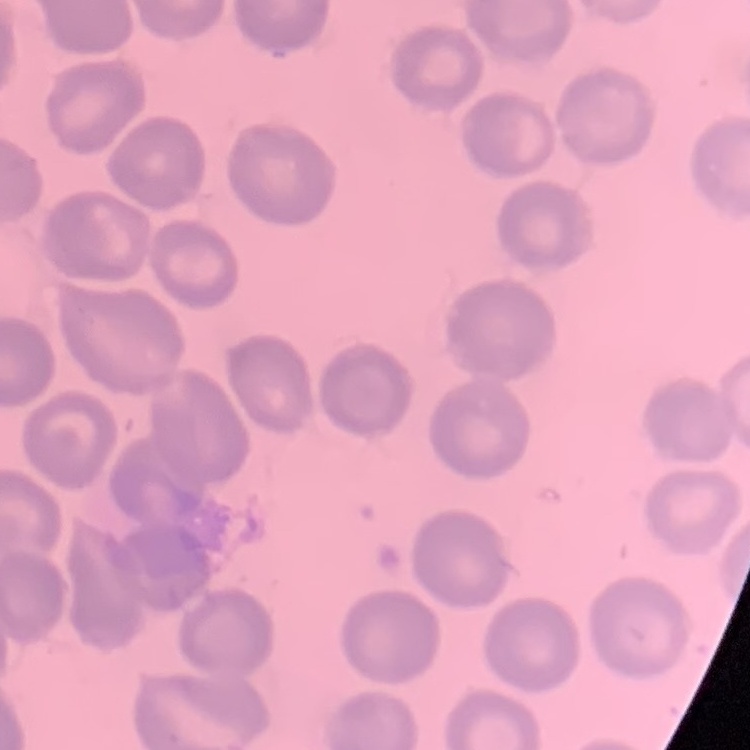
red blood cell morphology = no rouleaux formation
preparation = thin blood film
stain = Field's or Giemsa
image type = square crop of a larger photomicrograph